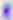

Summary:
  - Magnification: 400x
  - Modality: photomicrograph
  - Identification: Toxoplasma gondii